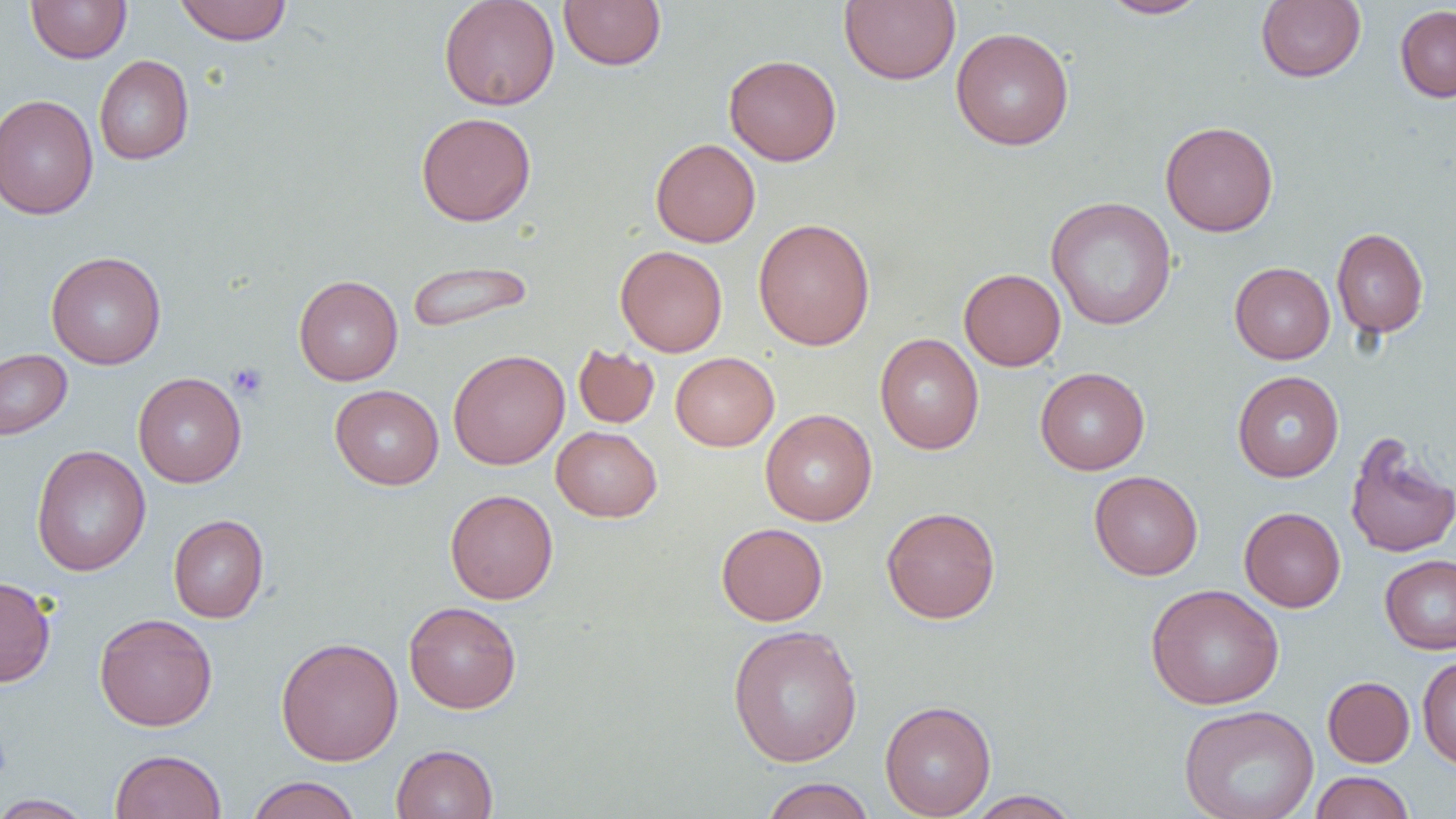

Summary:
  - Coordinate format: approximate bounding boxes as [x1, y1, x2, y2] in pixels
  - Platelet locations: [227, 362, 268, 400]
  - Uninfected red blood cell locations: [26, 0, 131, 63], [174, 0, 292, 45], [439, 0, 560, 111], [559, 0, 666, 70], [839, 0, 960, 85], [1097, 0, 1211, 19], [1256, 0, 1366, 82], [1395, 4, 1456, 103], [950, 27, 1074, 151], [723, 54, 842, 166], [94, 55, 194, 165], [0, 94, 99, 219], [416, 111, 536, 226], [1159, 120, 1278, 237], [650, 138, 760, 247], [1045, 195, 1177, 331], [753, 218, 875, 350], [1331, 227, 1429, 338], [615, 245, 728, 357], [46, 251, 166, 369], [406, 259, 533, 334], [1229, 262, 1335, 364], [959, 268, 1066, 371], [294, 275, 403, 385], [875, 333, 984, 454], [573, 344, 659, 428], [0, 349, 72, 441], [448, 349, 569, 470], [670, 352, 779, 451], [1035, 367, 1149, 475], [1232, 371, 1344, 481], [133, 372, 246, 487], [330, 384, 444, 489], [760, 409, 877, 525], [552, 426, 662, 521], [1344, 432, 1455, 559], [31, 445, 151, 576], [1089, 470, 1203, 580], [445, 489, 558, 604], [881, 506, 1001, 624], [1239, 507, 1346, 612], [168, 514, 269, 623], [716, 522, 828, 626], [1380, 554, 1456, 654], [0, 576, 56, 687], [1145, 583, 1284, 710], [403, 601, 522, 713], [94, 613, 217, 731], [727, 624, 864, 767], [276, 637, 403, 766], [1417, 656, 1456, 770], [1323, 676, 1414, 767], [879, 700, 996, 818], [1179, 704, 1319, 819], [391, 744, 498, 819], [110, 749, 226, 819], [1310, 771, 1414, 818], [245, 776, 361, 819], [760, 777, 876, 819], [965, 790, 1082, 818], [0, 794, 96, 818]
  - Slide-level diagnosis: negative for blood parasites
  - Modality: light microscopy
  - Magnification: 1000x
  - Preparation: thin blood smear
  - Image size: 1456×819 pixels
  - Field of view: single